Outline each blood parasite and name the species.
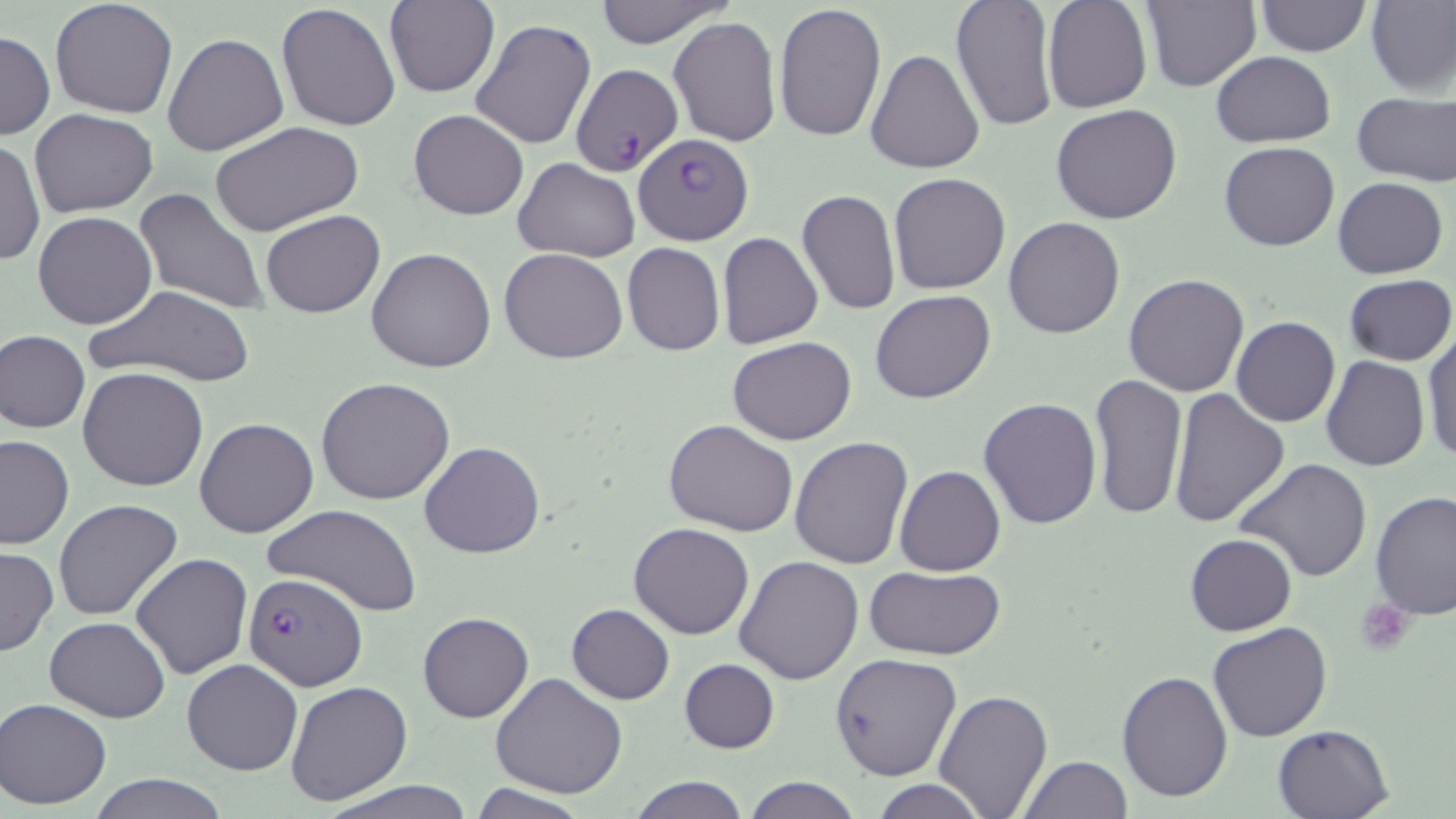

Approximate bounding boxes as named x1/y1/x2/y2 corners in pixels.
Plasmodium falciparum-infected red blood cells: (x1=570, y1=65, x2=680, y2=174), (x1=635, y1=133, x2=754, y2=244), (x1=242, y1=574, x2=366, y2=688).
No Plasmodium ovale, Plasmodium malariae, Plasmodium vivax, Babesia divergens, or Trypanosoma brucei observed.

Uninfected red blood cell locations: (x1=49, y1=0, x2=179, y2=120), (x1=590, y1=0, x2=737, y2=47), (x1=950, y1=0, x2=1058, y2=132), (x1=1043, y1=0, x2=1152, y2=113), (x1=1256, y1=0, x2=1369, y2=56), (x1=386, y1=1, x2=498, y2=98), (x1=1137, y1=1, x2=1261, y2=90), (x1=1366, y1=1, x2=1456, y2=96), (x1=773, y1=2, x2=885, y2=141), (x1=277, y1=4, x2=401, y2=132), (x1=667, y1=15, x2=782, y2=147), (x1=471, y1=19, x2=596, y2=149), (x1=0, y1=30, x2=53, y2=140), (x1=162, y1=32, x2=289, y2=157), (x1=865, y1=49, x2=984, y2=174), (x1=1211, y1=50, x2=1335, y2=147), (x1=1352, y1=92, x2=1456, y2=185), (x1=1051, y1=104, x2=1183, y2=224), (x1=31, y1=108, x2=158, y2=216), (x1=409, y1=109, x2=529, y2=221), (x1=210, y1=122, x2=363, y2=239), (x1=2, y1=137, x2=43, y2=269), (x1=1219, y1=141, x2=1340, y2=251), (x1=513, y1=158, x2=639, y2=261), (x1=888, y1=172, x2=1011, y2=294), (x1=1333, y1=178, x2=1447, y2=278), (x1=135, y1=187, x2=270, y2=315), (x1=797, y1=189, x2=900, y2=317), (x1=33, y1=210, x2=159, y2=329), (x1=260, y1=210, x2=385, y2=317), (x1=1004, y1=216, x2=1125, y2=338), (x1=718, y1=232, x2=824, y2=350), (x1=622, y1=243, x2=725, y2=355), (x1=366, y1=247, x2=497, y2=373), (x1=500, y1=247, x2=628, y2=364), (x1=1123, y1=273, x2=1249, y2=395), (x1=1344, y1=274, x2=1456, y2=365), (x1=83, y1=284, x2=256, y2=388), (x1=870, y1=289, x2=996, y2=404), (x1=1230, y1=316, x2=1340, y2=427), (x1=1, y1=329, x2=90, y2=433), (x1=1421, y1=329, x2=1455, y2=465), (x1=727, y1=337, x2=857, y2=445), (x1=1321, y1=356, x2=1429, y2=472), (x1=78, y1=367, x2=209, y2=492), (x1=1089, y1=372, x2=1189, y2=521), (x1=315, y1=377, x2=456, y2=505), (x1=1168, y1=387, x2=1288, y2=527), (x1=979, y1=397, x2=1102, y2=530), (x1=194, y1=418, x2=320, y2=539), (x1=665, y1=419, x2=799, y2=538), (x1=0, y1=435, x2=74, y2=550), (x1=789, y1=437, x2=914, y2=571), (x1=419, y1=441, x2=545, y2=558), (x1=1231, y1=458, x2=1374, y2=585), (x1=895, y1=465, x2=1004, y2=577), (x1=1370, y1=492, x2=1456, y2=620), (x1=54, y1=499, x2=183, y2=622), (x1=261, y1=503, x2=420, y2=617), (x1=628, y1=522, x2=755, y2=640), (x1=1185, y1=533, x2=1296, y2=636), (x1=1, y1=545, x2=57, y2=655), (x1=131, y1=554, x2=252, y2=678), (x1=733, y1=555, x2=863, y2=685), (x1=865, y1=566, x2=1005, y2=661), (x1=567, y1=604, x2=675, y2=704), (x1=418, y1=611, x2=533, y2=723), (x1=45, y1=616, x2=171, y2=721), (x1=1205, y1=622, x2=1332, y2=741), (x1=441, y1=653, x2=570, y2=791), (x1=829, y1=653, x2=962, y2=780), (x1=181, y1=659, x2=302, y2=775), (x1=680, y1=659, x2=780, y2=753), (x1=1116, y1=669, x2=1233, y2=802), (x1=490, y1=673, x2=628, y2=798), (x1=285, y1=680, x2=414, y2=806), (x1=933, y1=687, x2=1053, y2=817), (x1=1, y1=697, x2=112, y2=810), (x1=1270, y1=722, x2=1393, y2=818), (x1=1019, y1=755, x2=1131, y2=818), (x1=89, y1=773, x2=229, y2=819), (x1=627, y1=776, x2=750, y2=819), (x1=321, y1=777, x2=477, y2=819), (x1=744, y1=777, x2=862, y2=818), (x1=871, y1=778, x2=987, y2=818), (x1=466, y1=783, x2=592, y2=819). Platelet locations: (x1=1357, y1=599, x2=1413, y2=653). Slide-level diagnosis: Plasmodium falciparum. Thin blood film. One field of a larger specimen. May-Grünwald-Giemsa stain. Light microscopy. Image is 1456×819 pixels. Captured at 1000x magnification.